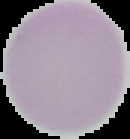
Summary:
  - Preparation: thin blood film
  - Malaria status: uninfected
  - Image size: 130×139 pixels
  - Image type: cell region segmented out of the field of view; surrounding area masked to black